Outline platelets.
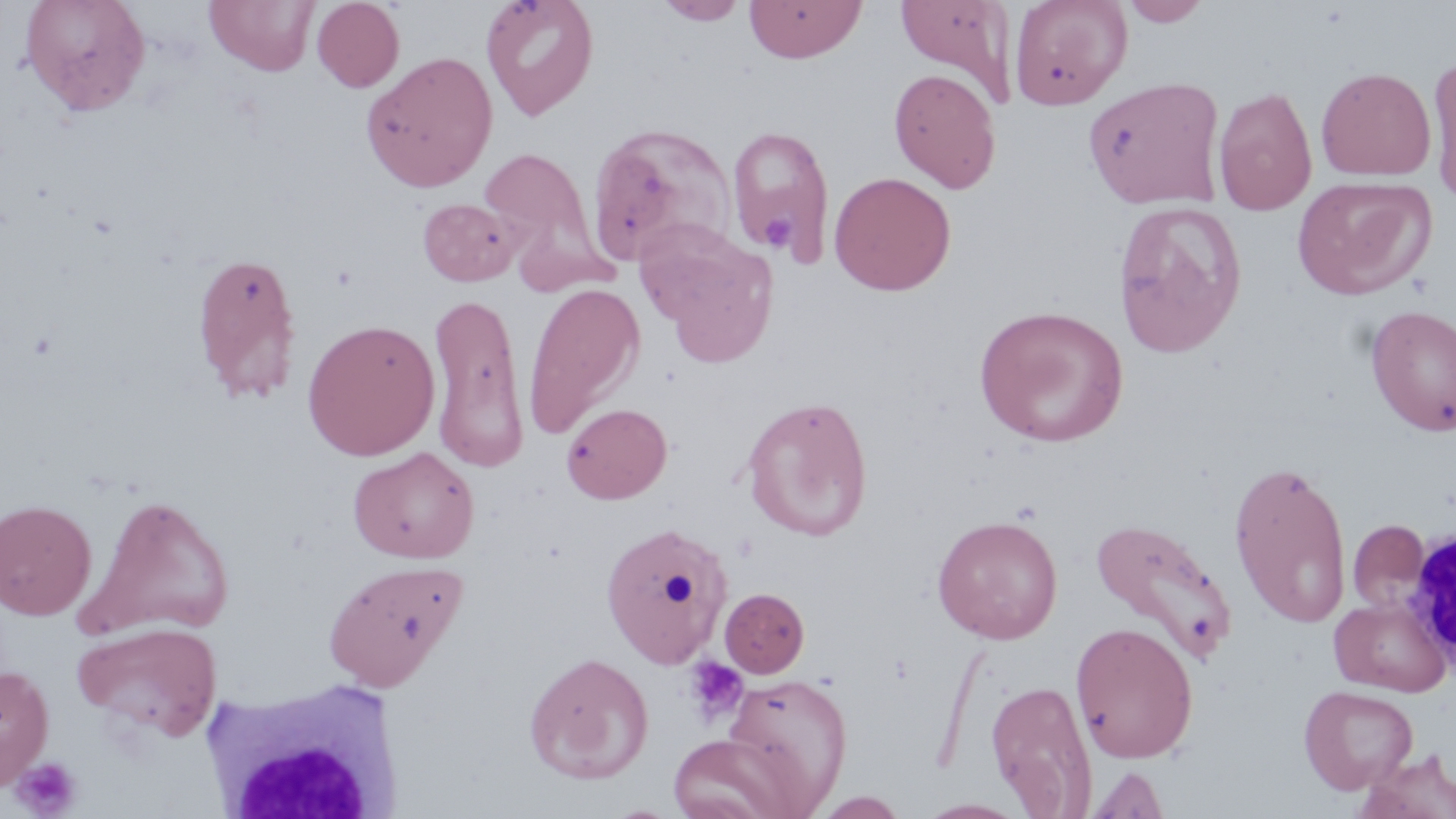
Approximate bounding boxes as [x1, y1, x2, y2] in pixels.
Platelets: [761, 212, 796, 252], [684, 656, 750, 725], [10, 756, 83, 817].

Summary:
  - Uninfected red blood cell locations: [19, 0, 151, 116], [204, 0, 319, 76], [312, 0, 404, 92], [480, 0, 600, 121], [743, 0, 867, 63], [894, 0, 1018, 106], [1009, 0, 1132, 110], [1118, 0, 1213, 26], [655, 1, 749, 25], [361, 51, 498, 192], [1427, 54, 1456, 206], [1316, 66, 1436, 181], [888, 67, 1002, 194], [1083, 76, 1226, 209], [1213, 85, 1317, 215], [586, 122, 737, 267], [726, 124, 836, 262], [479, 146, 604, 278], [829, 171, 956, 295], [1293, 175, 1435, 299], [417, 198, 522, 286], [1113, 200, 1248, 357], [634, 219, 780, 363], [191, 250, 303, 404], [522, 283, 645, 438], [428, 291, 530, 472], [973, 304, 1129, 447], [1365, 304, 1456, 436], [301, 318, 440, 461], [741, 395, 873, 540], [562, 402, 672, 503], [349, 447, 479, 563], [1228, 459, 1352, 629], [79, 494, 235, 639], [0, 498, 97, 619], [932, 514, 1063, 644], [1089, 515, 1237, 666], [1348, 519, 1430, 615], [599, 520, 735, 668], [323, 559, 468, 691], [719, 587, 810, 679], [1329, 596, 1452, 697], [72, 621, 221, 741], [1070, 621, 1199, 763], [523, 651, 654, 784], [0, 663, 54, 790], [722, 672, 853, 809], [986, 678, 1098, 816], [1298, 685, 1418, 794], [666, 732, 804, 819], [1355, 748, 1456, 819], [1087, 765, 1170, 818], [811, 791, 910, 818], [915, 798, 1030, 818]
  - White blood cell locations: [1401, 528, 1455, 669], [202, 672, 409, 819]
  - Slide-level diagnosis: no evidence of blood parasites
  - Preparation: thin blood smear
  - Field of view: single
  - Modality: optical microscopy
  - Stain: May-Grünwald-Giemsa
  - Magnification: 1000x
  - Image size: 1456×819 pixels